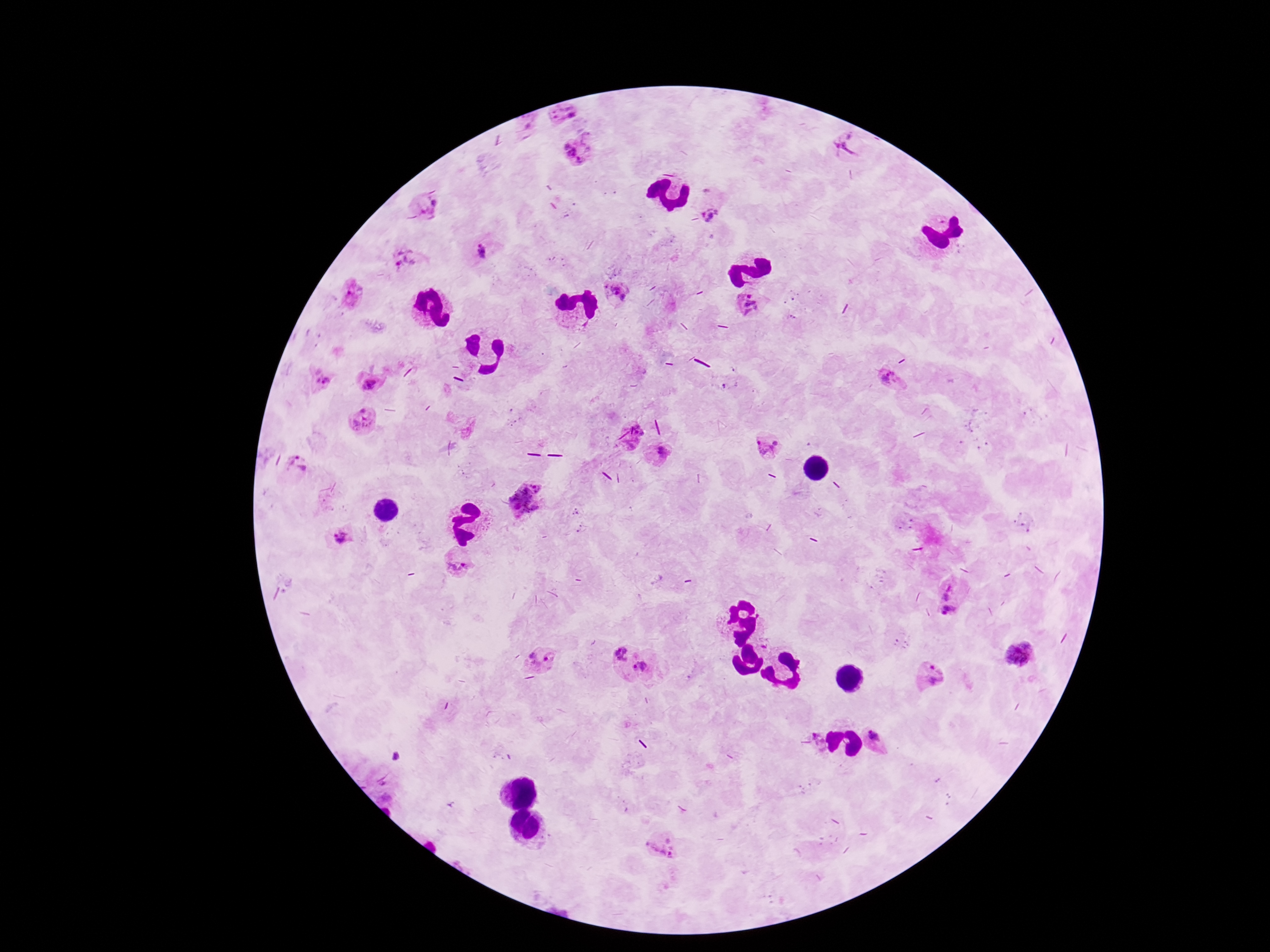

image size = 1270×952 pixels
field of view = one from this slide
Plasmodium parasite locations = approximate centers as (x, y) in pixels: (562, 115), (851, 141), (579, 149), (429, 206), (713, 214), (480, 251), (404, 264), (614, 291), (352, 293), (749, 303), (368, 382), (321, 383), (890, 383), (360, 421), (768, 447), (659, 453), (293, 466), (525, 501), (341, 540), (457, 564), (951, 597), (617, 651), (1019, 654), (540, 660), (642, 666), (927, 674), (877, 739), (821, 741), (661, 851)
preparation = thick peripheral-blood smear
magnification = 100x
patient malaria status = infected
capture = smartphone camera through the microscope eyepiece
stain = Giemsa